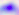
Summary:
  - Magnification: 400x
  - Identification: Toxoplasma gondii
  - Modality: micrograph